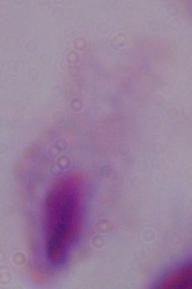

{
  "modality": "photomicrograph",
  "identification": "trichomonad",
  "magnification": "1000x"
}